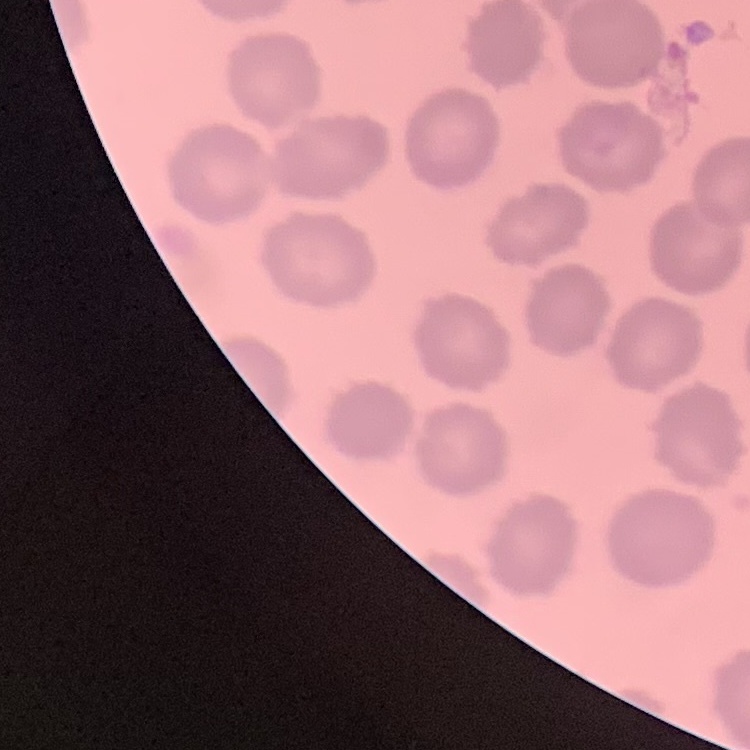

Summary:
  - Red blood cell morphology: no rouleaux formation
  - Image type: square crop of a larger photomicrograph
  - Stain: Field's or Giemsa
  - Preparation: thin blood smear